Assess this cell for malaria.
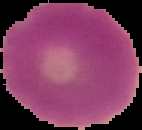
It is uninfected.

Image is 142×130 pixels. From a thin blood smear. Cell region segmented out of the field of view; the surrounding area is masked to black.